Describe the morphology of the erythrocytes.
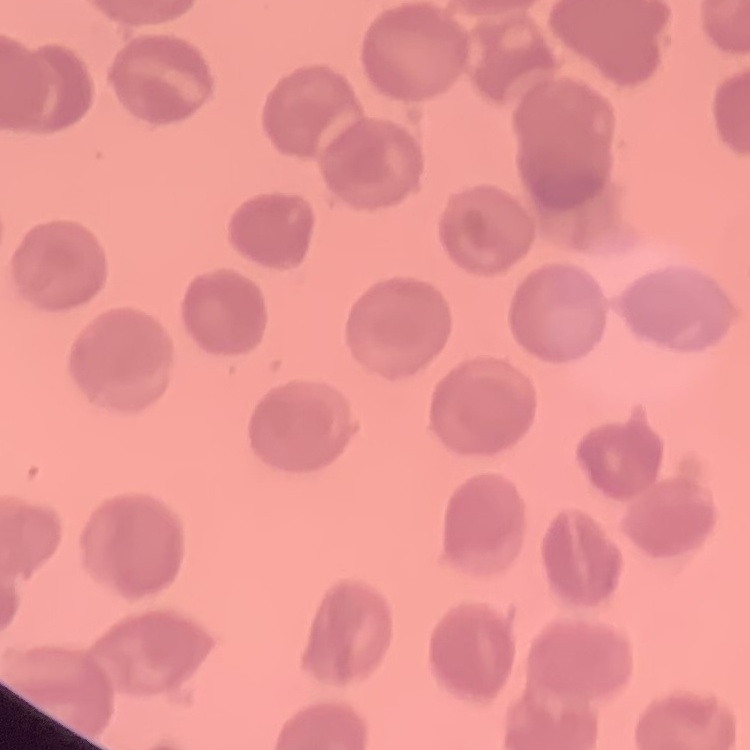

They show no rouleaux formation.

Thin blood film. Field's or Giemsa stain. Square crop of a larger photomicrograph.